Name the parasite shown.
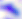

This is Toxoplasma gondii.

modality = photomicrograph
magnification = 400x